Identify the cell.
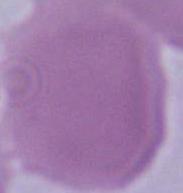

This is an erythrocyte.

{
  "modality": "micrograph",
  "magnification": "1000x"
}